Classify this cell by malaria status.
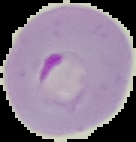

It is parasitized.

{
  "image_size": "136×142 pixels",
  "preparation": "thin blood film",
  "image_type": "segmented cell region with the area outside set to black"
}